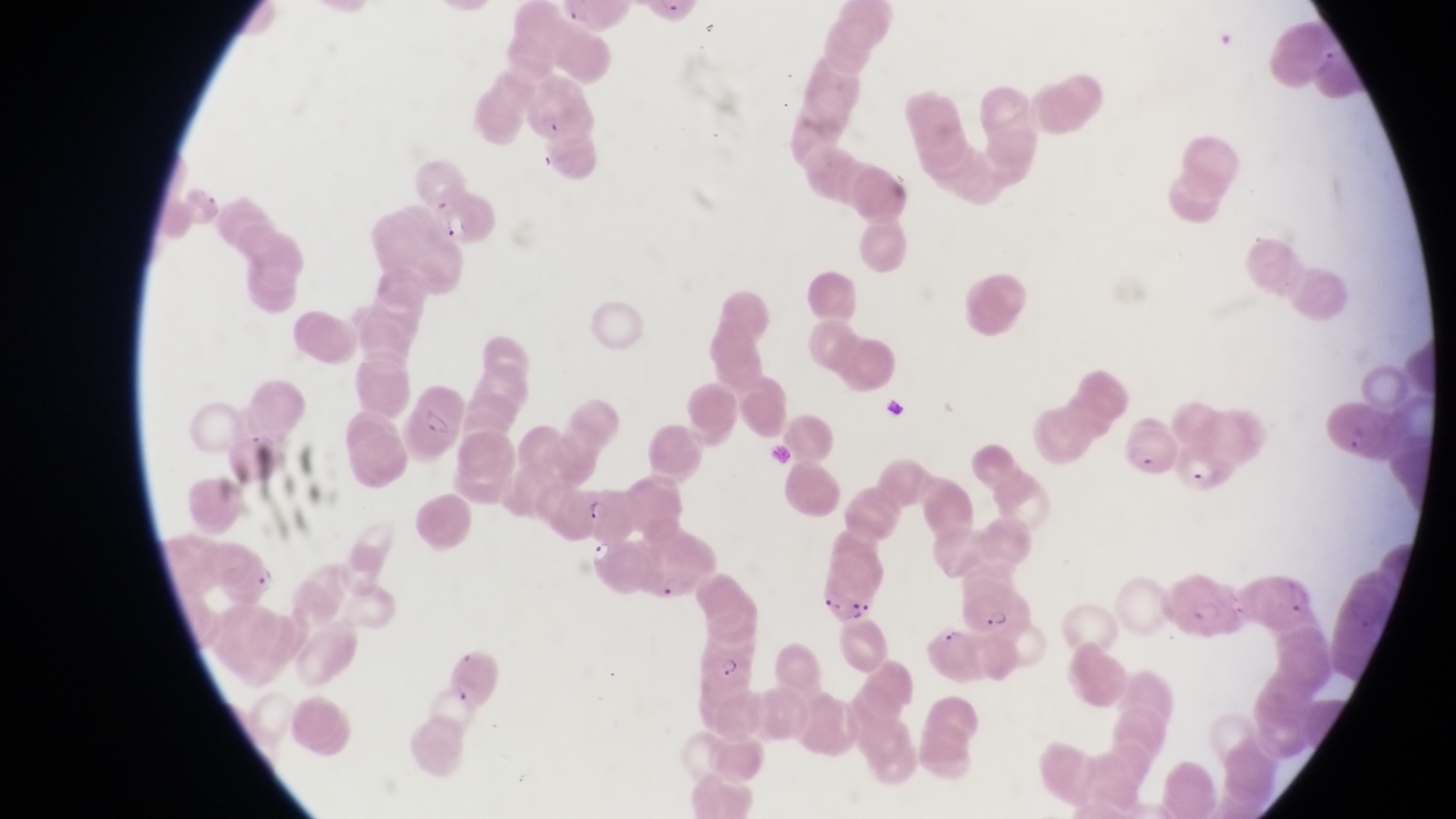
Approximate bounding boxes as (left, top, right, bottom) in pixels.
Summary:
  - Trophozoite locations: (587, 542, 617, 569), (249, 566, 282, 592)
  - Parasitised red blood cell locations: (523, 82, 595, 145), (436, 190, 503, 249), (403, 396, 464, 459), (1329, 396, 1395, 460), (1131, 419, 1178, 480), (1181, 436, 1242, 499), (571, 483, 629, 538), (817, 558, 877, 625), (1169, 570, 1239, 637), (962, 582, 1026, 634), (693, 632, 760, 690)
  - Preparation: thin blood smear
  - Capture: smartphone photograph through the eyepiece of an Olympus CX-23 microscope
  - Magnification: 1000x
  - Country: Uganda
  - Image size: 1456×819 pixels
  - Field of view: single